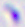

identification: Toxoplasma gondii
modality: photomicrograph
magnification: 400x